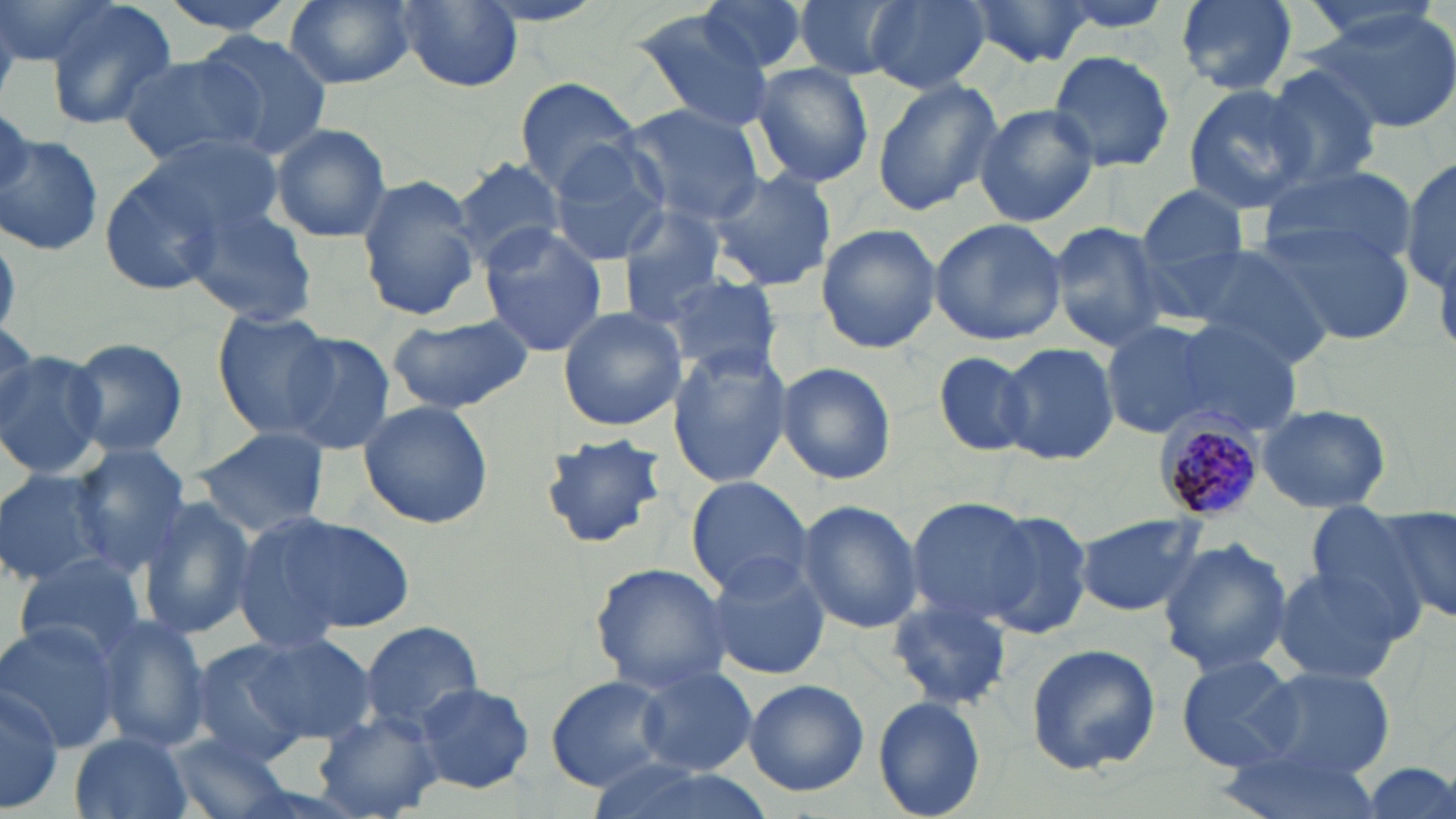
Summary:
  - Coordinate format: approximate bounding boxes as [x1, y1, x2, y2] in pixels
  - Plasmodium malariae-infected red blood cell locations: [1156, 413, 1267, 525]
  - Uninfected red blood cell locations: [1, 0, 115, 69], [153, 0, 308, 37], [285, 0, 415, 90], [697, 0, 816, 77], [794, 0, 909, 84], [866, 0, 989, 92], [961, 0, 1096, 70], [1166, 0, 1300, 95], [1294, 0, 1449, 46], [41, 1, 178, 131], [391, 1, 523, 92], [1312, 7, 1456, 134], [628, 12, 782, 133], [195, 31, 334, 160], [1048, 50, 1175, 173], [119, 51, 267, 166], [1259, 64, 1386, 193], [751, 65, 873, 187], [516, 76, 644, 195], [870, 79, 1002, 215], [1182, 84, 1315, 215], [974, 102, 1099, 228], [621, 105, 767, 227], [270, 123, 392, 243], [140, 133, 285, 241], [1, 134, 104, 258], [546, 138, 673, 266], [450, 156, 567, 269], [1402, 158, 1456, 291], [1259, 166, 1415, 268], [705, 168, 837, 291], [98, 170, 220, 297], [357, 178, 480, 322], [1138, 185, 1250, 274], [183, 202, 318, 326], [616, 203, 732, 319], [928, 217, 1067, 347], [1260, 218, 1415, 346], [1048, 220, 1169, 353], [816, 224, 942, 355], [476, 227, 610, 357], [1183, 244, 1335, 367], [656, 271, 782, 378], [556, 305, 689, 431], [212, 312, 338, 436], [383, 314, 536, 413], [1100, 319, 1216, 439], [1163, 320, 1302, 437], [0, 324, 49, 426], [278, 334, 395, 455], [66, 337, 189, 460], [998, 342, 1121, 466], [666, 344, 792, 489], [934, 350, 1039, 456], [0, 351, 107, 480], [775, 362, 897, 485], [357, 398, 494, 530], [1254, 402, 1394, 514], [193, 426, 331, 536], [541, 434, 668, 549], [66, 445, 190, 574], [0, 468, 116, 590], [684, 475, 813, 598], [139, 497, 257, 641], [905, 497, 1037, 622], [795, 499, 924, 634], [1372, 506, 1456, 623], [1297, 507, 1431, 620], [975, 508, 1094, 641], [1074, 511, 1206, 616], [263, 512, 417, 634], [229, 514, 359, 656], [1157, 537, 1293, 677], [701, 553, 832, 679], [12, 554, 149, 667], [589, 563, 732, 691], [1270, 565, 1412, 684], [886, 596, 1014, 711], [96, 614, 211, 755], [0, 618, 126, 752], [360, 621, 484, 736], [233, 632, 378, 744], [186, 640, 314, 765], [1024, 641, 1162, 774], [1173, 653, 1307, 772], [1240, 664, 1396, 786], [635, 665, 757, 776], [545, 674, 670, 790], [0, 678, 64, 814], [743, 678, 869, 797], [412, 681, 538, 794], [873, 695, 988, 819], [314, 711, 445, 818], [68, 731, 197, 819], [163, 733, 301, 819], [1215, 746, 1386, 819], [1358, 762, 1454, 819]
  - Slide-level diagnosis: Plasmodium malariae
  - Stain: May-Grünwald-Giemsa
  - Magnification: 1000x
  - Preparation: thin blood smear
  - Field of view: one of a larger specimen
  - Modality: optical microscopy
  - Image size: 1456×819 pixels